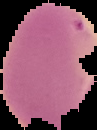 Image is 97×130 pixels. Cell region segmented out of the field of view; the surrounding area is masked to black. From a thin blood smear. Malaria status: uninfected.